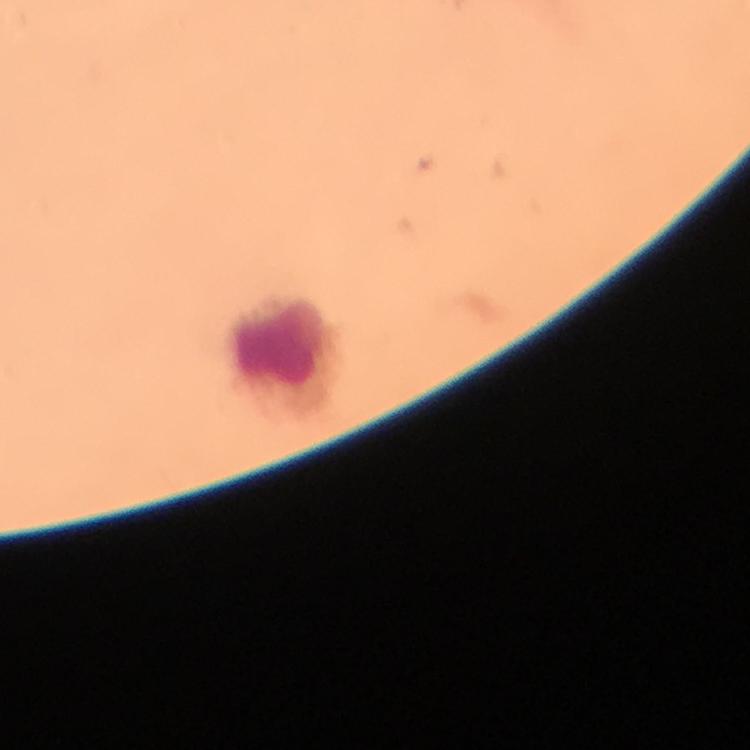
Approximate centers as (x, y) in pixels. Leukocyte locations: (278, 341). Giemsa stain. Plasmodium parasites: none seen. From a malaria diagnostic workup. At 100x magnification. A crop from one field of view. Thick smear. Immersion oil applied. Image is 750×750 pixels. Smartphone photograph taken through a microscope.